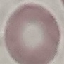

malaria status = uninfected
stain = Giemsa
capture = smartphone through the microscope eyepiece
preparation = thin smear
image type = automatically extracted cell patch, resized to 64 × 64 pixels